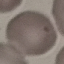
Summary:
  - Malaria status: uninfected
  - Capture: smartphone camera at the microscope eyepiece
  - Stain: Giemsa
  - Image type: cell patch, automatically extracted from a larger field of view and resized to 64 × 64 pixels
  - Preparation: thin blood film